Assess this cell for malaria.
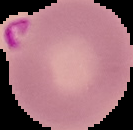
It is parasitized.

image type = segmented cell region with the area outside set to black
image size = 133×130 pixels
preparation = thin blood smear